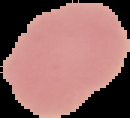
Malaria status: uninfected. Image is 130×118 pixels. From a thin blood film. The area outside the segmented cell region is set to black.